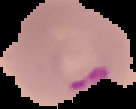

Malaria status: parasitized. From a thin blood film. Image is 136×109 pixels. Segmented cell region on a black background.